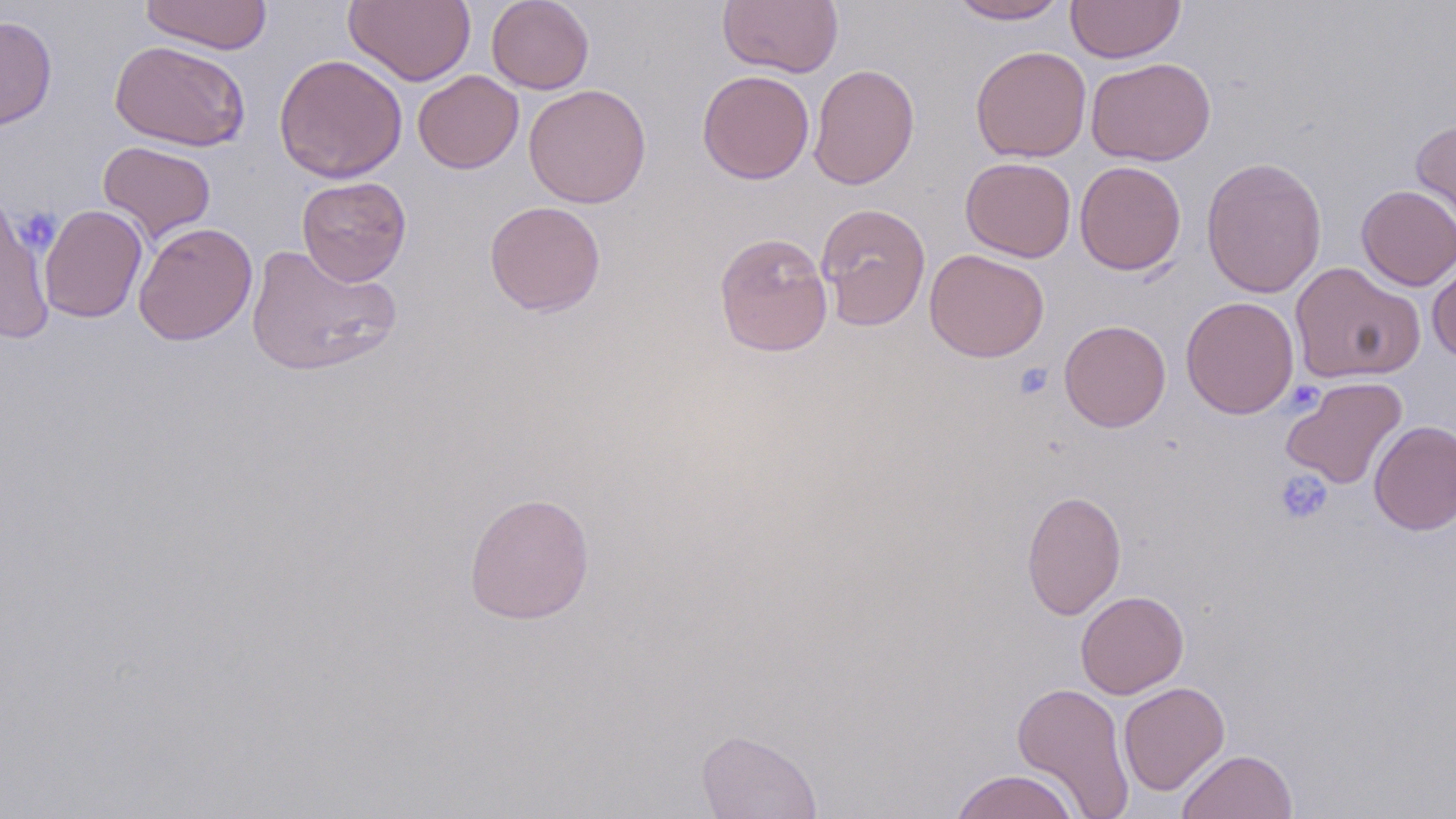
slide-level diagnosis = negative for blood parasites
magnification = 1000x
uninfected red blood cell locations = approximate bounding boxes as [x1, y1, x2, y2] in pixels: [138, 0, 273, 55], [343, 0, 475, 86], [486, 0, 594, 94], [717, 0, 844, 77], [948, 0, 1069, 24], [1066, 0, 1185, 63], [0, 15, 57, 131], [109, 40, 250, 152], [970, 45, 1091, 162], [274, 53, 408, 183], [1086, 57, 1216, 166], [808, 64, 920, 190], [697, 69, 815, 184], [413, 70, 524, 174], [523, 84, 652, 209], [1410, 118, 1456, 243], [98, 140, 216, 244], [1201, 156, 1327, 298], [960, 157, 1076, 262], [1074, 160, 1187, 275], [296, 176, 412, 286], [1356, 184, 1456, 290], [0, 194, 54, 344], [484, 200, 606, 316], [815, 202, 931, 331], [39, 204, 148, 323], [133, 222, 258, 345], [713, 231, 833, 358], [245, 243, 401, 377], [924, 248, 1050, 363], [1427, 257, 1456, 362], [1289, 261, 1426, 384], [1180, 296, 1300, 419], [1059, 320, 1171, 432], [1281, 376, 1408, 490], [1369, 420, 1456, 535], [1021, 489, 1126, 620], [463, 492, 595, 624], [1075, 590, 1189, 698], [1118, 681, 1229, 796], [1011, 682, 1135, 818], [696, 729, 822, 818], [1177, 749, 1298, 819], [950, 768, 1079, 819]
image size = 1456×819 pixels
preparation = thin blood film
field of view = one of a larger specimen
modality = light microscopy
stain = May-Grünwald-Giemsa
platelet locations = approximate bounding boxes as [x1, y1, x2, y2] in pixels: [1013, 362, 1054, 401], [1273, 470, 1333, 526]